Assess this cell for malaria.
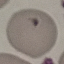
It is uninfected.

Summary:
  - Stain: Giemsa
  - Image type: automatically extracted cell patch, resized to 64 × 64 pixels
  - Preparation: thin blood smear
  - Capture: smartphone through the microscope eyepiece